Assess this cell for malaria.
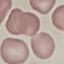

Uninfected.

preparation = thin blood film
image type = cell patch, automatically extracted from a larger field of view and resized to 64 × 64 pixels
capture = smartphone through the microscope eyepiece
stain = Giemsa